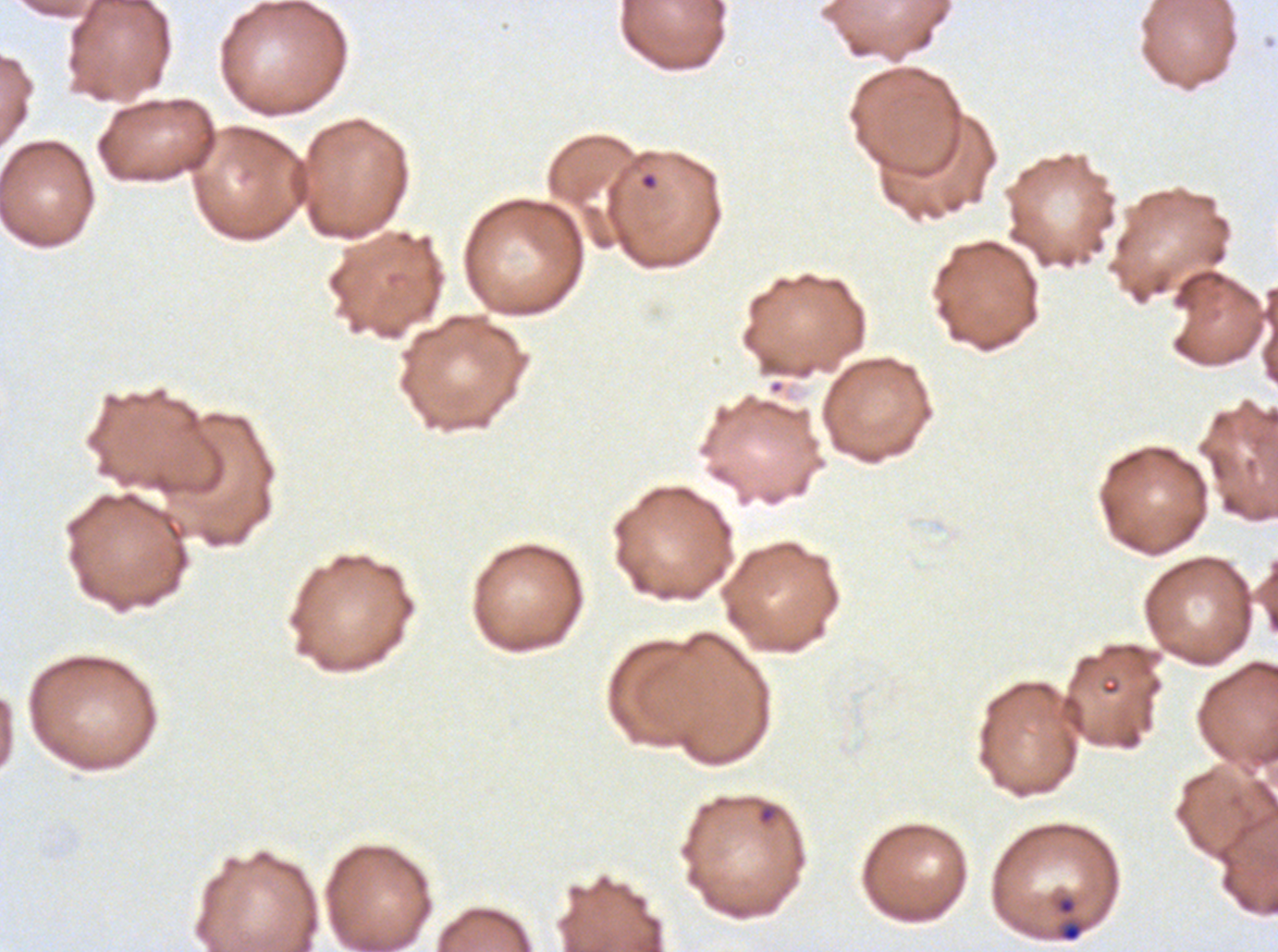
Approximate bounding rectangles given as corner coordinates in pixels from the top-left.
Summary:
  - Ring locations: (x1=639, y1=172, x2=658, y2=190), (x1=756, y1=801, x2=780, y2=827), (x1=1052, y1=893, x2=1088, y2=944)
  - Field of view: one sub-image of a larger composite
  - Image size: 1278×952 pixels
  - Preparation: thin blood film
  - Stain: Giemsa
  - Specimen: P. falciparum cultured ex vivo for 24 to 48 hours, from a patient in The Gambia